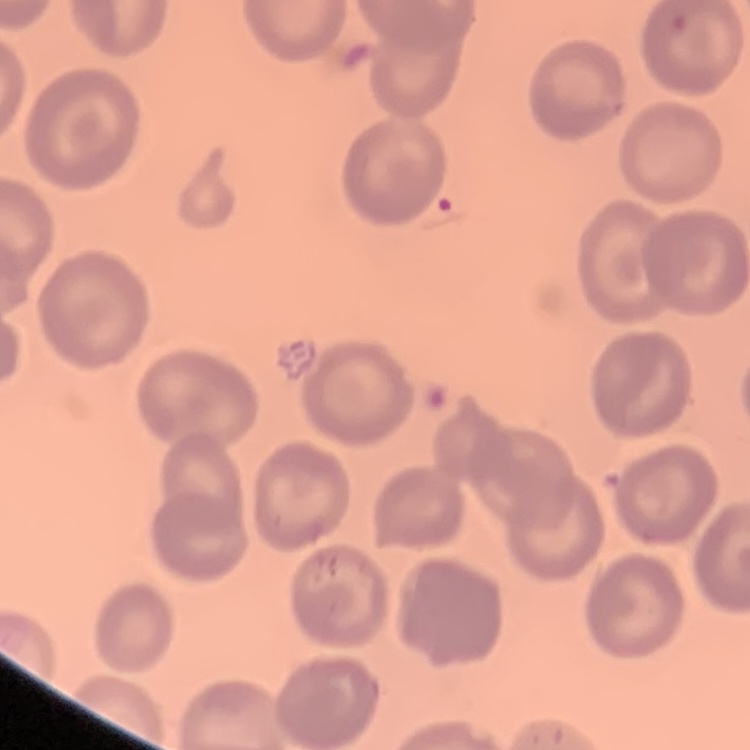

Summary:
  - Erythrocyte morphology: no rouleaux formation
  - Image type: square crop of a larger photomicrograph
  - Preparation: thin blood film
  - Stain: Field's or Giemsa